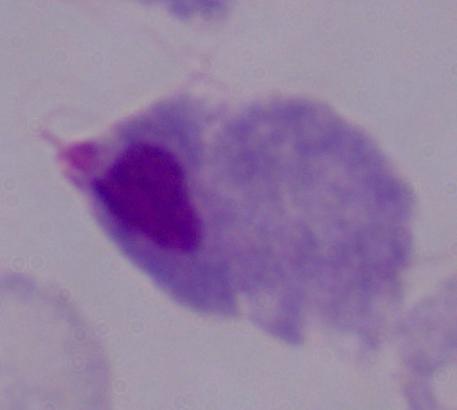

{
  "modality": "photomicrograph",
  "magnification": "1000x",
  "identification": "trichomonad"
}